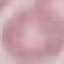

Malaria status: uninfected. Thin smear of blood. Giemsa stain. Photographed with a smartphone camera at the microscope eyepiece. Cell patch, automatically extracted from a larger field of view and resized to 64 × 64 pixels.